Describe the morphology of the erythrocytes.
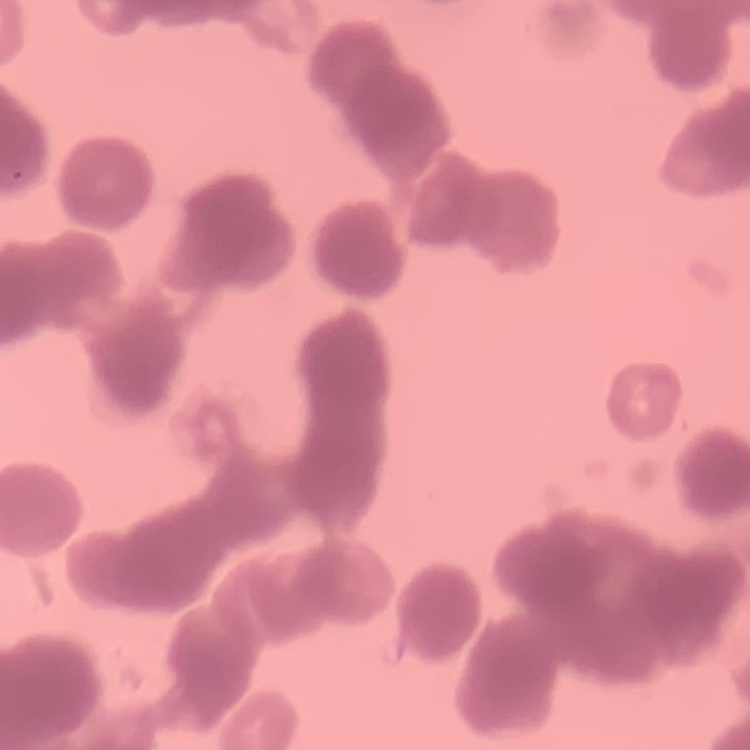
They show rouleaux formation.

Summary:
  - Image type: one tile cut from a larger photomicrograph
  - Preparation: thin peripheral smear
  - Stain: Field's or Giemsa